Assess the morphology of the erythrocytes.
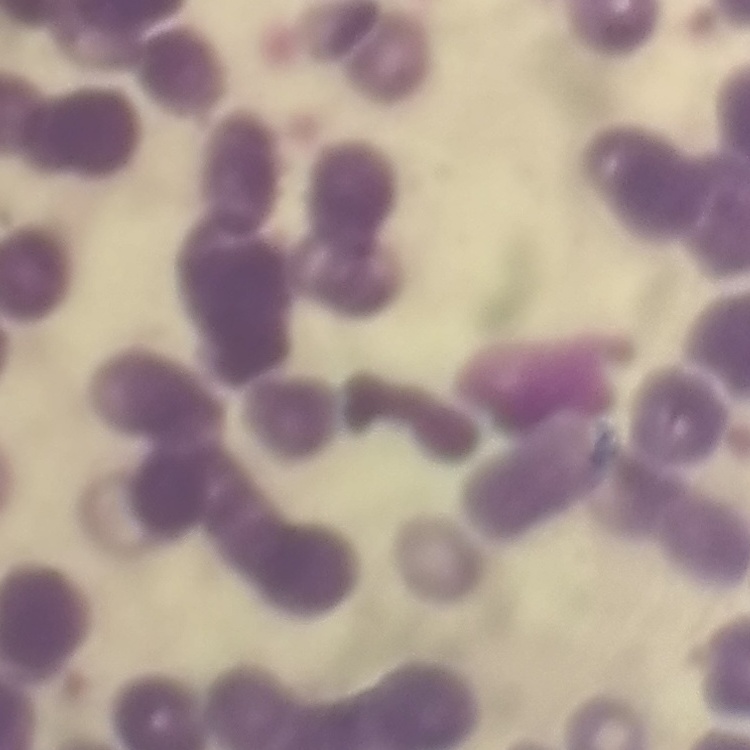

They show rouleaux formation.

{
  "preparation": "thin blood film",
  "image_type": "square crop of a larger photomicrograph",
  "stain": "Field's or Giemsa"
}